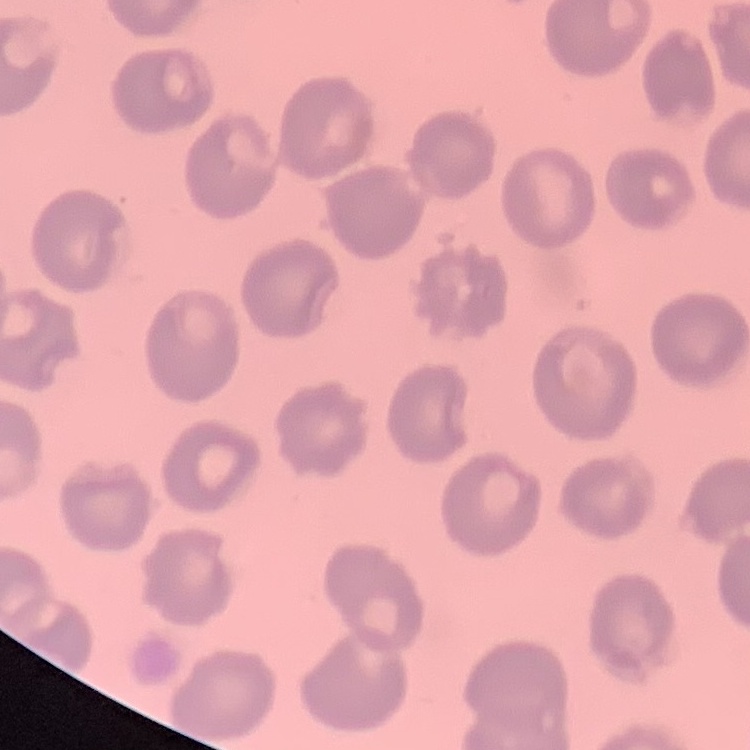
Summary:
  - Red blood cell morphology: no rouleaux formation
  - Image type: one tile cut from a larger photomicrograph
  - Preparation: thin peripheral smear
  - Stain: Field's or Giemsa